Assess this cell for malaria.
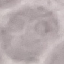
It is uninfected.

preparation = thin smear
image type = automatically extracted cell patch, resized to 64 × 64 pixels
capture = smartphone camera at the microscope eyepiece
stain = Giemsa